Describe the morphology of the erythrocytes.
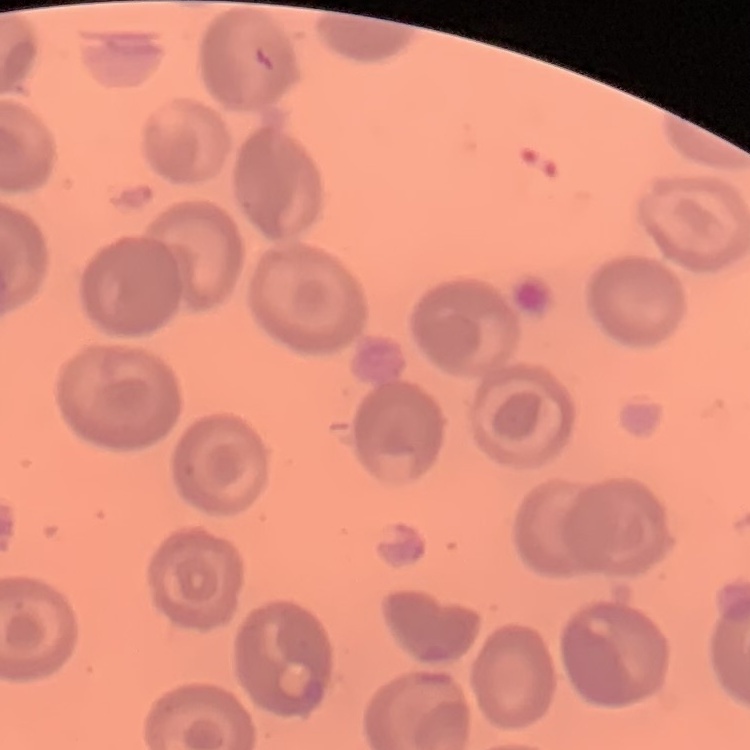
No rouleaux formation.

Summary:
  - Stain: Field's or Giemsa
  - Image type: square crop of a larger photomicrograph
  - Preparation: thin blood film